Describe the morphology of the erythrocytes.
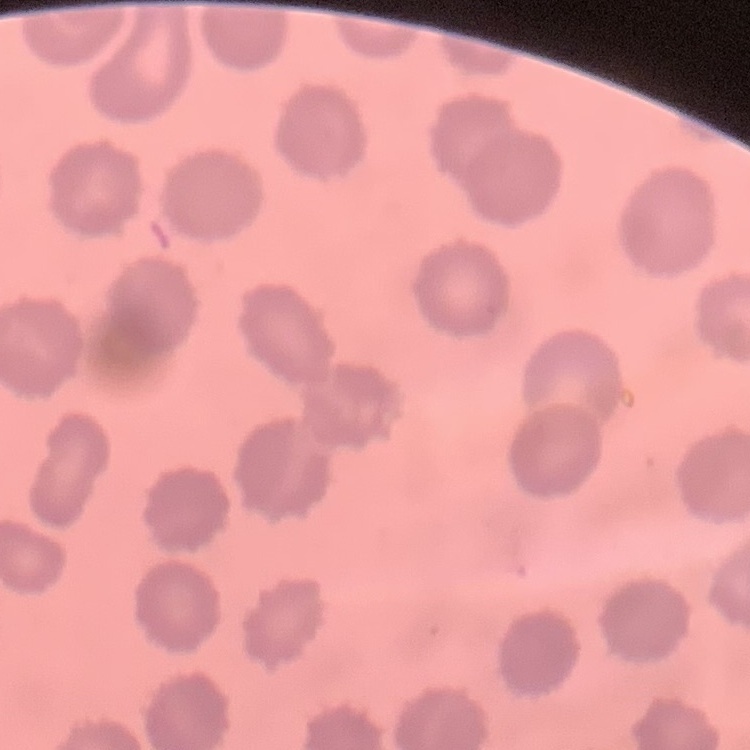
No rouleaux formation.

Summary:
  - Preparation: thin blood smear
  - Image type: one tile cut from a larger photomicrograph
  - Stain: Field's or Giemsa